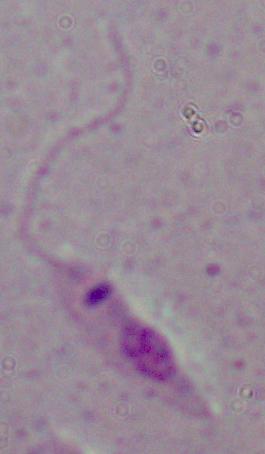
1000x magnification. Photomicrograph. A Leishmania parasite is seen.